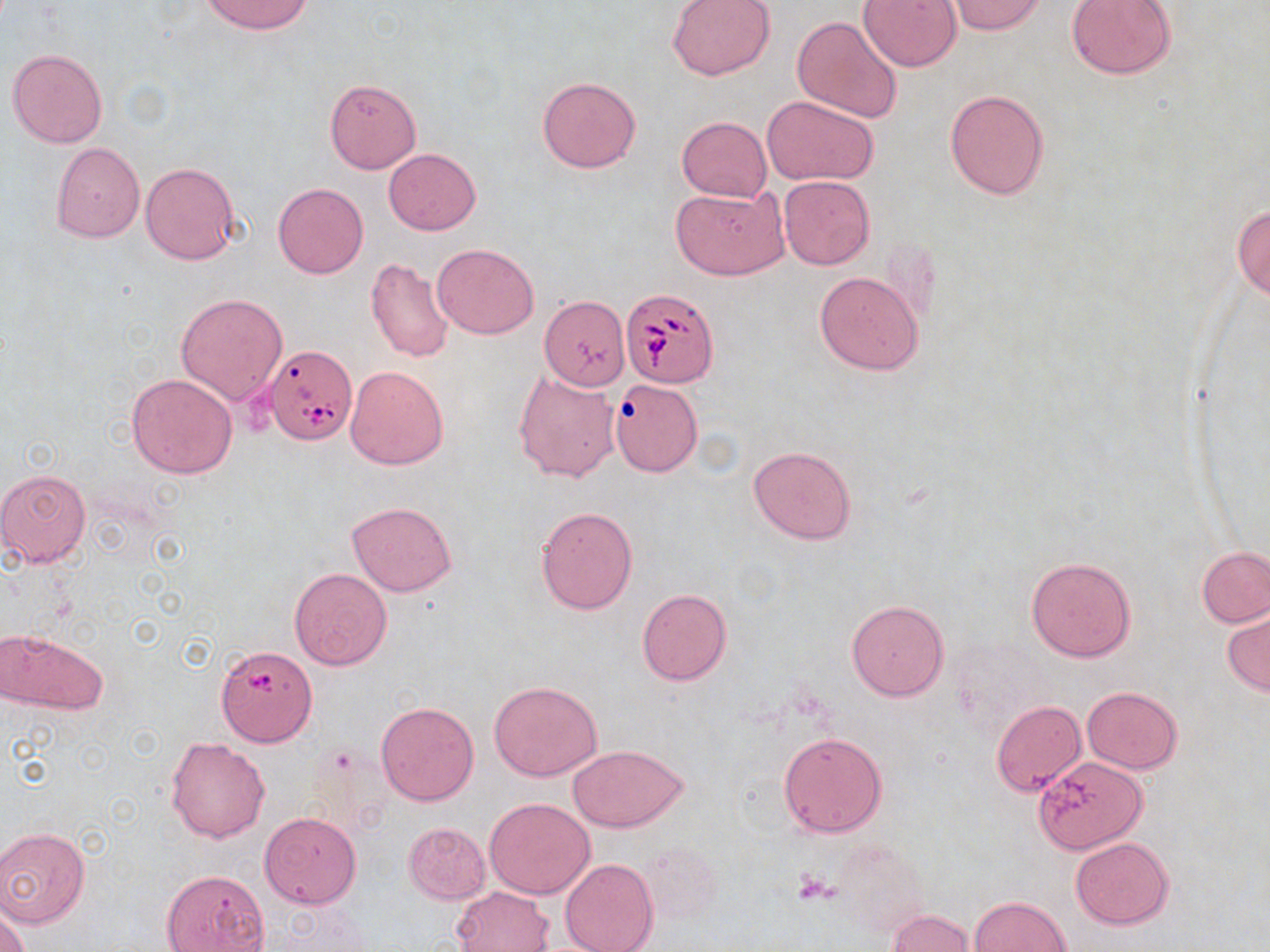

Summary:
  - Coordinate format: approximate bounding boxes as (x1, y1, x2, y2) in pixels
  - Platelet locations: (795, 872, 838, 905)
  - Uninfected red blood cell locations: (201, 0, 314, 35), (666, 0, 775, 80), (858, 0, 963, 72), (1067, 0, 1176, 79), (948, 1, 1048, 34), (792, 16, 905, 123), (8, 48, 108, 149), (537, 76, 641, 172), (324, 79, 421, 173), (944, 88, 1050, 200), (762, 95, 880, 186), (677, 116, 772, 201), (51, 142, 145, 242), (384, 148, 481, 234), (141, 162, 240, 265), (779, 175, 874, 270), (273, 183, 368, 279), (670, 185, 789, 280), (1232, 204, 1270, 301), (432, 242, 539, 339), (364, 255, 454, 363), (814, 270, 925, 375), (175, 292, 288, 404), (540, 298, 627, 392), (345, 364, 451, 469), (513, 367, 620, 482), (127, 373, 238, 477), (609, 380, 703, 476), (748, 445, 857, 545), (0, 469, 91, 568), (346, 501, 456, 597), (535, 506, 638, 615), (1198, 547, 1270, 628), (1025, 556, 1136, 662), (289, 568, 393, 672), (637, 588, 732, 685), (845, 600, 949, 700), (1223, 606, 1270, 695), (0, 629, 109, 715), (218, 649, 317, 750), (489, 680, 603, 782), (1082, 687, 1181, 773), (992, 700, 1085, 796), (375, 701, 480, 806), (777, 732, 888, 838), (166, 738, 270, 843), (568, 744, 688, 833), (1032, 757, 1147, 857), (485, 798, 595, 899), (259, 812, 362, 909), (403, 822, 490, 904), (0, 827, 90, 929), (833, 837, 930, 938), (1070, 837, 1174, 928), (639, 840, 721, 926), (561, 857, 657, 952), (161, 869, 271, 952), (449, 886, 555, 952), (970, 895, 1071, 951), (0, 902, 31, 952), (886, 909, 975, 952)
  - Babesia divergens-infected red blood cell locations: (620, 288, 719, 388), (265, 346, 357, 446)
  - Slide-level diagnosis: Babesia divergens
  - Image size: 1270×952 pixels
  - Field of view: one of a larger specimen
  - Preparation: thin blood smear
  - Modality: optical microscopy
  - Magnification: 1000x
  - Stain: May-Grünwald-Giemsa